Comment on the morphology of the red blood cells.
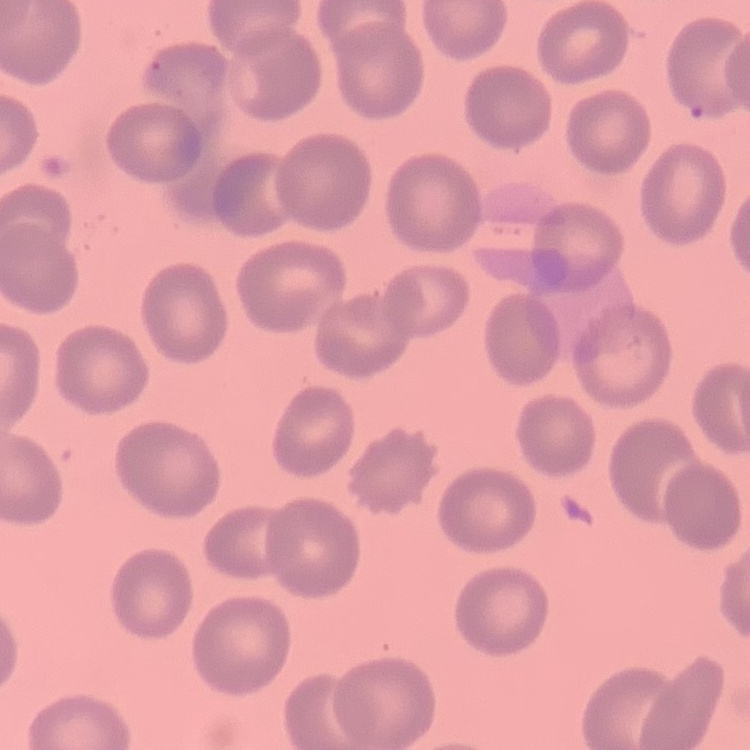

No rouleaux formation.

Summary:
  - Stain: Field's or Giemsa
  - Image type: square crop of a larger photomicrograph
  - Preparation: thin blood film